Report the malaria status of this cell.
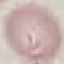
It is uninfected.

Acquired by smartphone through the microscope eyepiece. Giemsa stain. Thin smear of blood. Automatically extracted cell patch, resized to 64 × 64 pixels.